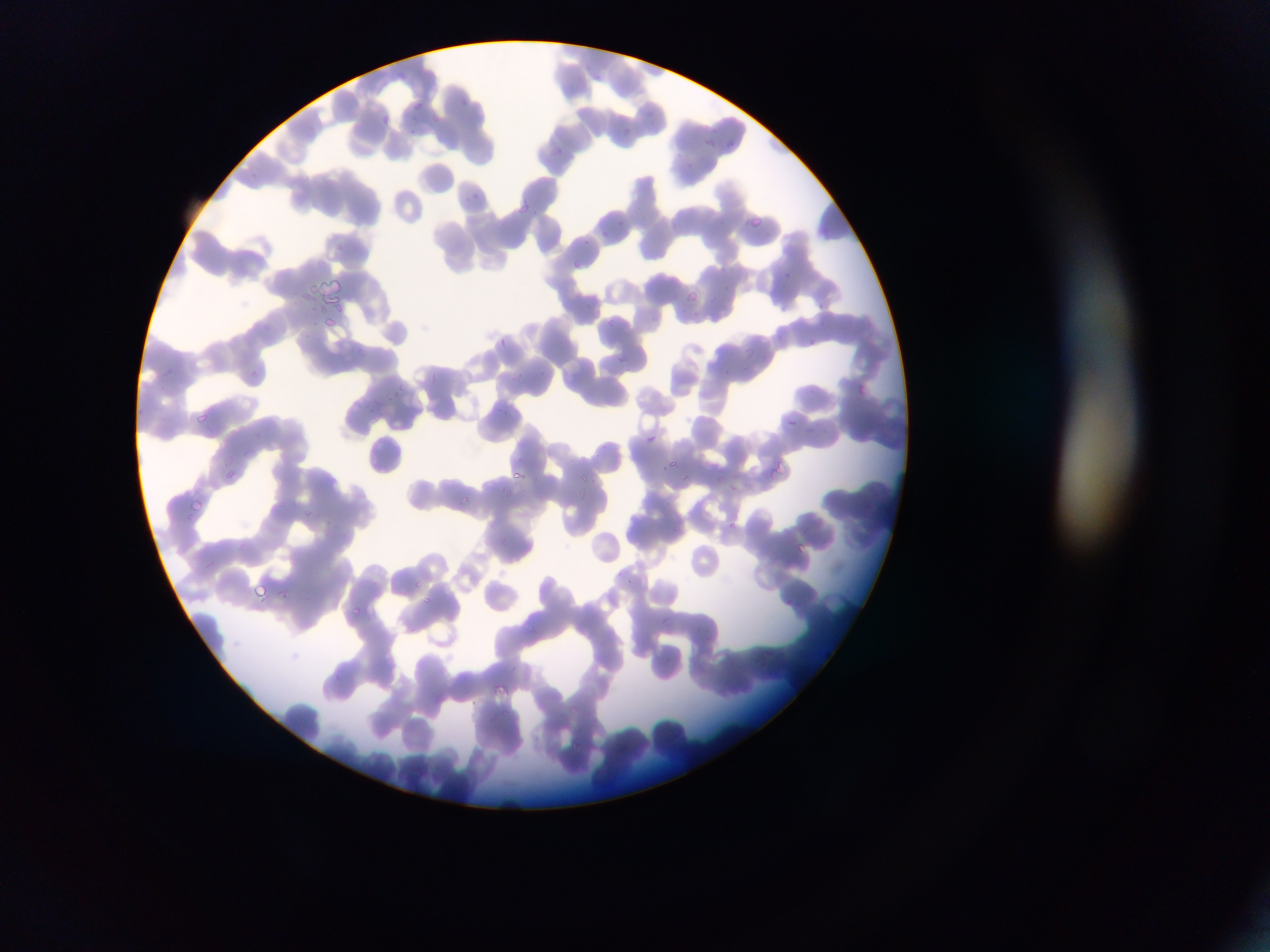 Approximate bounding boxes as {left, top, right, bottom} in pixels. Malaria parasite locations: {459, 95, 470, 109}, {414, 103, 423, 109}, {645, 107, 652, 115}, {375, 112, 394, 129}, {411, 125, 421, 137}, {624, 129, 634, 137}, {706, 137, 718, 147}, {729, 138, 738, 151}, {251, 171, 259, 179}, {470, 191, 482, 201}, {520, 203, 527, 213}, {752, 217, 766, 226}, {615, 219, 627, 229}, {602, 227, 612, 236}, {571, 260, 584, 268}, {782, 270, 790, 280}, {722, 285, 734, 293}, {301, 290, 315, 302}, {684, 290, 702, 298}, {816, 301, 830, 310}, {322, 315, 340, 331}, {607, 318, 616, 327}, {260, 326, 270, 332}, {497, 336, 509, 346}, {810, 336, 820, 348}, {744, 344, 757, 358}, {618, 358, 627, 363}, {741, 363, 748, 373}, {162, 369, 174, 376}, {519, 369, 529, 377}, {724, 369, 734, 379}, {430, 371, 444, 384}, {535, 371, 552, 377}, {853, 382, 869, 397}, {398, 383, 407, 391}, {386, 393, 395, 403}, {368, 403, 379, 417}, {493, 403, 511, 415}, {197, 412, 211, 423}, {786, 415, 802, 428}, {255, 430, 271, 440}, {647, 432, 661, 446}, {669, 458, 677, 467}, {773, 461, 788, 474}, {225, 469, 237, 479}, {515, 469, 527, 478}, {578, 471, 594, 483}, {685, 475, 696, 489}, {502, 485, 515, 499}, {458, 495, 474, 504}, {190, 496, 209, 510}, {306, 510, 319, 524}, {726, 521, 736, 528}, {670, 525, 686, 537}, {796, 544, 807, 552}, {411, 577, 429, 586}, {627, 577, 634, 587}, {253, 579, 271, 602}, {284, 591, 292, 600}, {422, 594, 434, 609}, {351, 603, 364, 615}, {494, 683, 509, 702} | approximate {x, y} pixel centers of objects too small to bound: {585, 240}, {780, 335}, {254, 372}. Thin blood film. Photographed through a microscope with a mobile-phone camera. One field of view. Sample from Ghana. Image is 1270×952 pixels.